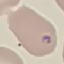
Summary:
  - Result: malaria parasites detected
  - Image type: automatically extracted cell patch, resized to 64 × 64 pixels
  - Capture: smartphone through the microscope eyepiece
  - Preparation: thin blood film
  - Stain: Giemsa